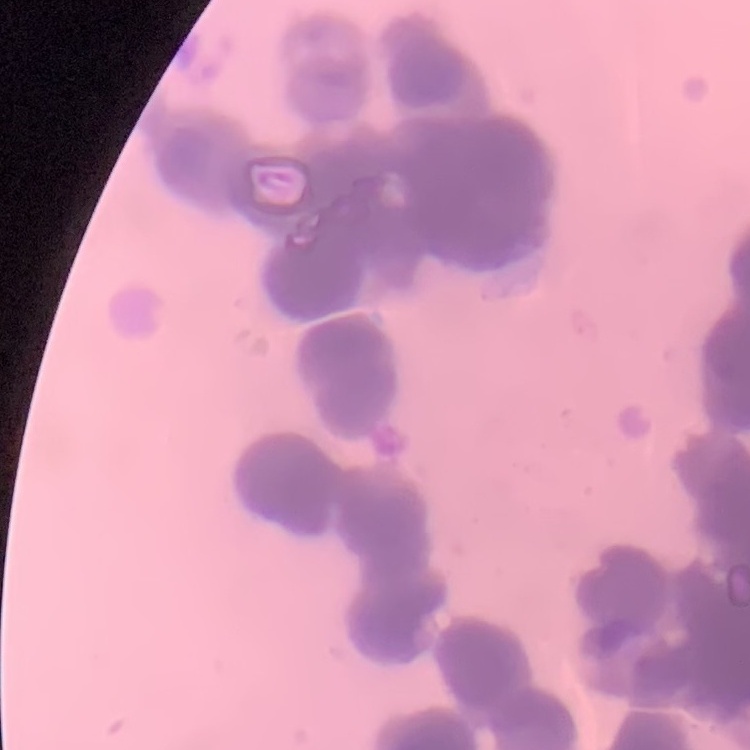
Summary:
  - Erythrocyte morphology: rouleaux formation
  - Image type: square crop of a larger photomicrograph
  - Stain: Field's or Giemsa
  - Preparation: thin blood smear